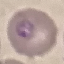

Result: malaria parasites identified. Cell patch, automatically extracted from a larger field of view and resized to 64 × 64 pixels. Photographed with a smartphone camera at the microscope eyepiece. Thin blood smear. Giemsa-stained preparation.